Comment on the morphology of the erythrocytes.
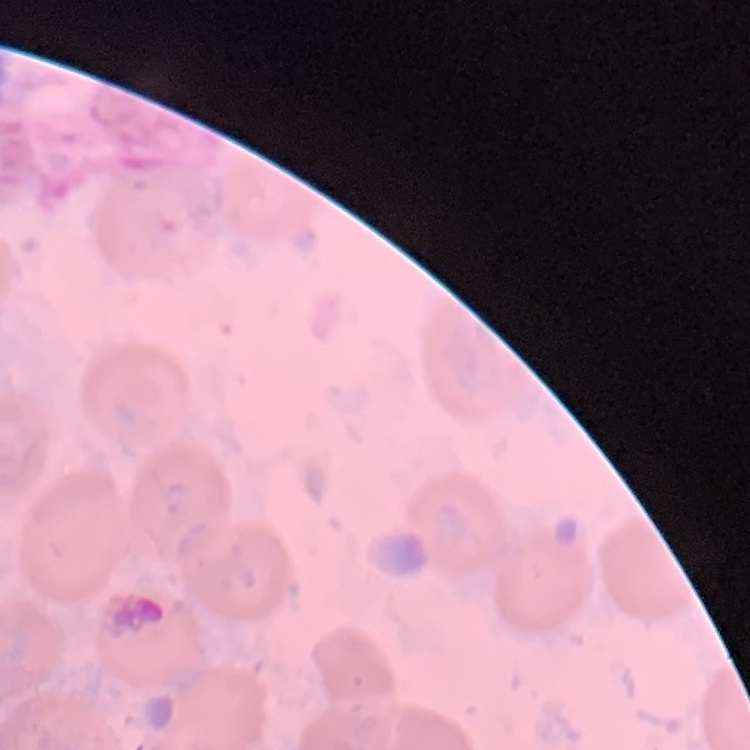

They show no rouleaux formation.

Square crop of a larger photomicrograph. Stained with either Field's or Giemsa. Thin peripheral smear.